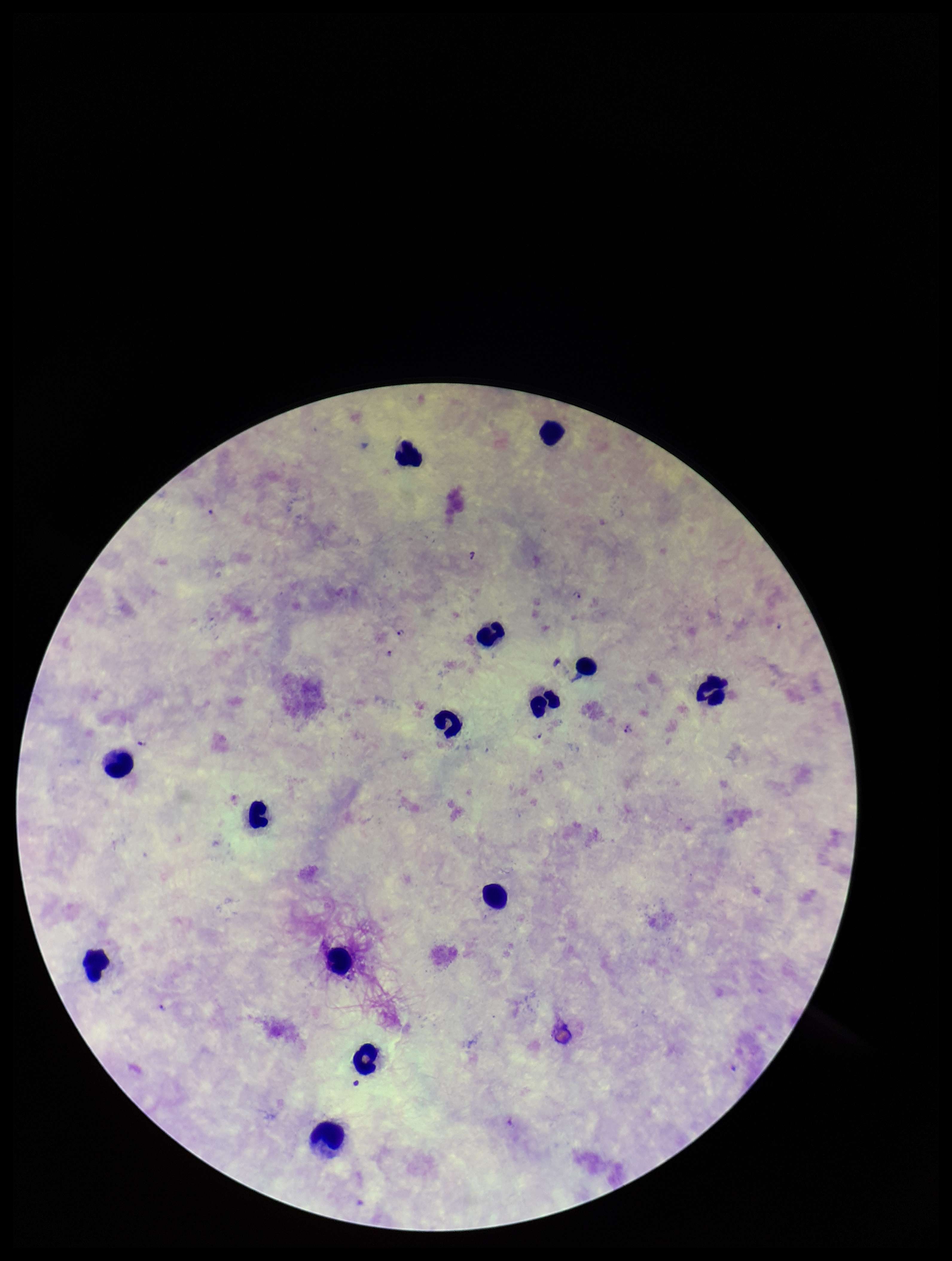
Photographed through the microscope eyepiece with a smartphone camera. Single field of view. Giemsa stain. Species reported for this patient: Plasmodium falciparum. Parasite count: 5. Image is 952×1261 pixels. Plasmodium parasites: detected. Patient malaria status: positive. Preparation: thick. Leukocyte count: 14.